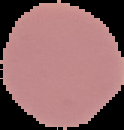

Summary:
  - Malaria status: uninfected
  - Image size: 124×130 pixels
  - Image type: segmented cell region on a black background
  - Preparation: thin blood smear